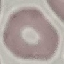
Summary:
  - Result: no malaria parasites seen
  - Preparation: thin blood film
  - Image type: automatically extracted cell patch, resized to 64 × 64 pixels
  - Stain: Giemsa
  - Capture: smartphone through the microscope eyepiece